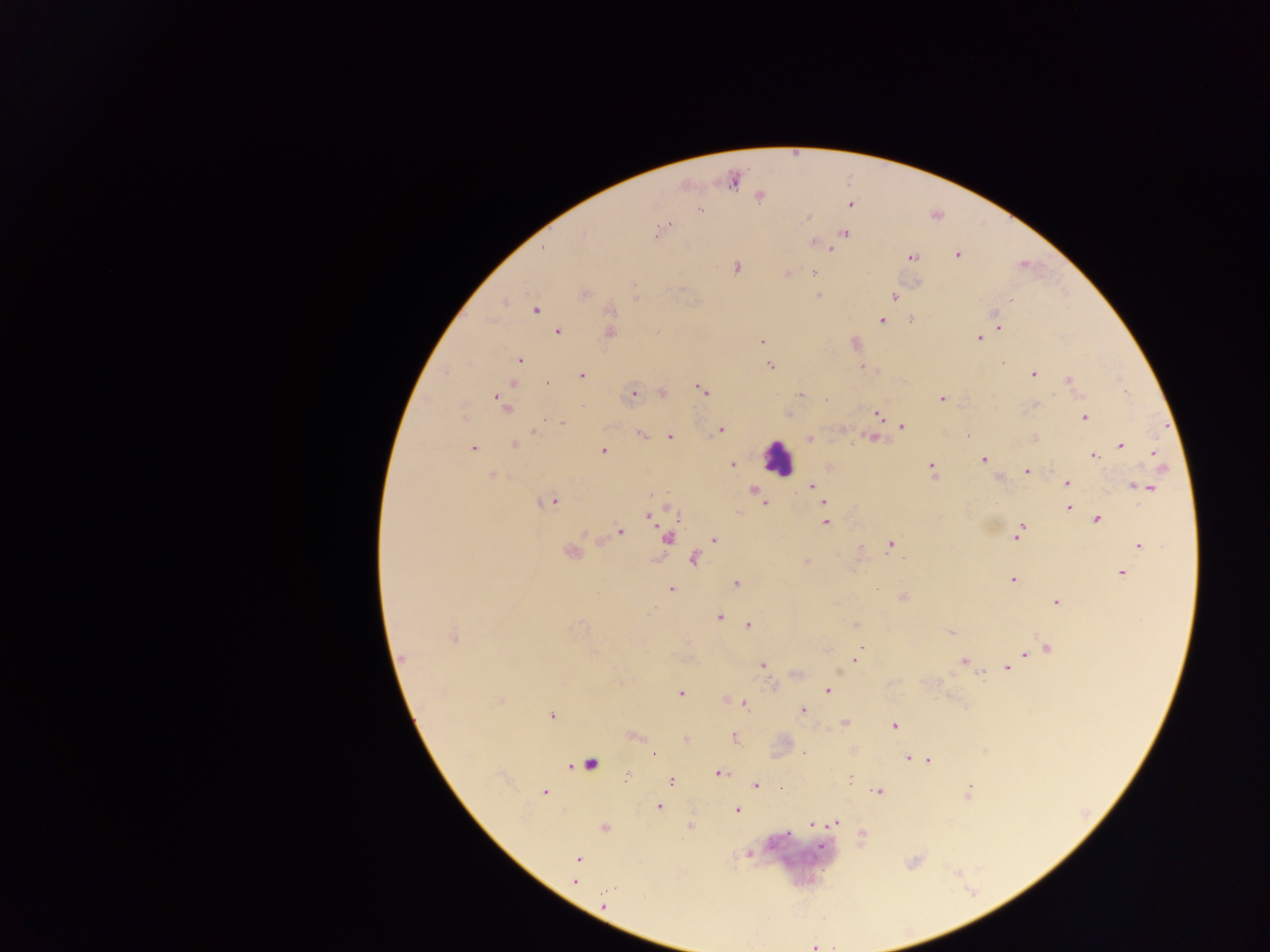
Approximate centers as {x, y} in pixels. Plasmodium parasite locations: {732, 179}, {759, 196}, {849, 204}, {699, 210}, {665, 228}, {844, 233}, {814, 241}, {542, 249}, {829, 249}, {957, 255}, {911, 257}, {735, 267}, {814, 273}, {787, 274}, {916, 282}, {583, 293}, {818, 295}, {892, 295}, {1009, 299}, {503, 301}, {535, 310}, {995, 317}, {911, 318}, {882, 320}, {998, 327}, {557, 331}, {609, 333}, {979, 337}, {762, 341}, {854, 343}, {519, 360}, {770, 364}, {863, 367}, {1033, 374}, {581, 375}, {1068, 380}, {513, 383}, {701, 389}, {662, 392}, {632, 393}, {800, 395}, {943, 397}, {826, 399}, {503, 404}, {1034, 405}, {878, 413}, {787, 414}, {1084, 416}, {560, 423}, {901, 426}, {720, 430}, {641, 434}, {669, 436}, {872, 437}, {810, 438}, {1035, 438}, {514, 444}, {1119, 445}, {472, 448}, {603, 450}, {1153, 453}, {1092, 455}, {983, 459}, {931, 465}, {732, 466}, {829, 466}, {1026, 470}, {932, 473}, {493, 475}, {998, 477}, {1067, 483}, {1133, 485}, {811, 486}, {1148, 487}, {752, 490}, {816, 490}, {760, 498}, {553, 500}, {764, 502}, {823, 502}, {1068, 507}, {671, 508}, {649, 516}, {1097, 519}, {825, 521}, {619, 532}, {1019, 532}, {667, 537}, {714, 540}, {891, 543}, {1139, 545}, {571, 551}, {694, 559}, {806, 561}, {1121, 573}, {1013, 579}, {735, 584}, {670, 589}, {901, 597}, {1056, 601}, {718, 617}, {748, 624}, {855, 625}, {951, 631}, {453, 637}, {862, 646}, {1046, 648}, {1036, 651}, {1025, 654}, {401, 659}, {853, 660}, {964, 661}, {762, 664}, {1006, 668}, {795, 674}, {827, 691}, {680, 693}, {500, 701}, {725, 701}, {743, 703}, {802, 711}, {551, 716}, {844, 723}, {893, 725}, {633, 737}, {734, 737}, {685, 740}, {852, 750}, {653, 756}, {907, 757}, {928, 760}, {589, 763}, {718, 772}, {628, 774}, {671, 780}, {849, 780}, {756, 785}, {779, 788}, {878, 791}, {544, 792}, {968, 792}, {659, 807}, {736, 809}, {835, 823}, {812, 824}, {689, 825}, {604, 827}, {861, 836}, {748, 853}, {577, 859}, {575, 881}, {604, 904}. Leukocyte locations: {778, 457}. Sample from Ghana. Thick blood film. Image is 1270×952 pixels. Single field of view. Photographed through a microscope with a mobile-phone camera.